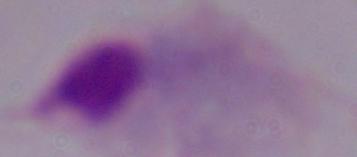
Captured at 1000x magnification. Micrograph. A trichomonad is seen.